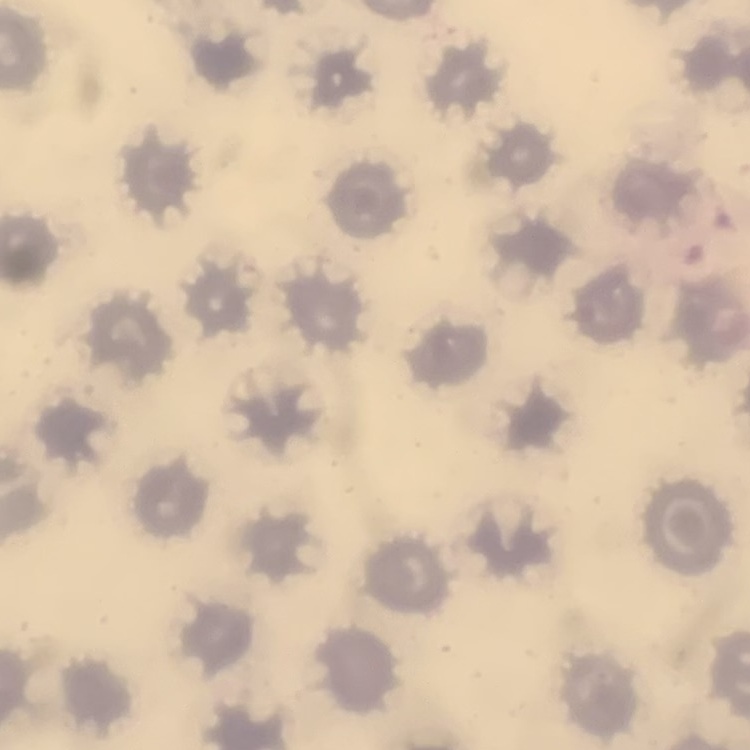 The red blood cells show no rouleaux formation. Thin blood smear. Stained with either Field's or Giemsa. One tile cut from a larger photomicrograph.